Assess this cell for malaria.
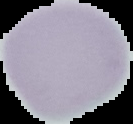
Uninfected.

Summary:
  - Image type: segmented cell region on a black background
  - Preparation: thin blood film
  - Image size: 133×124 pixels